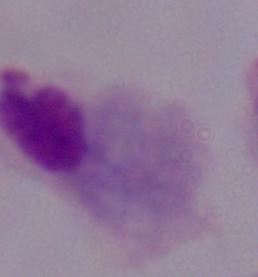

Captured at 1000x magnification. A trichomonad is seen. Photomicrograph.